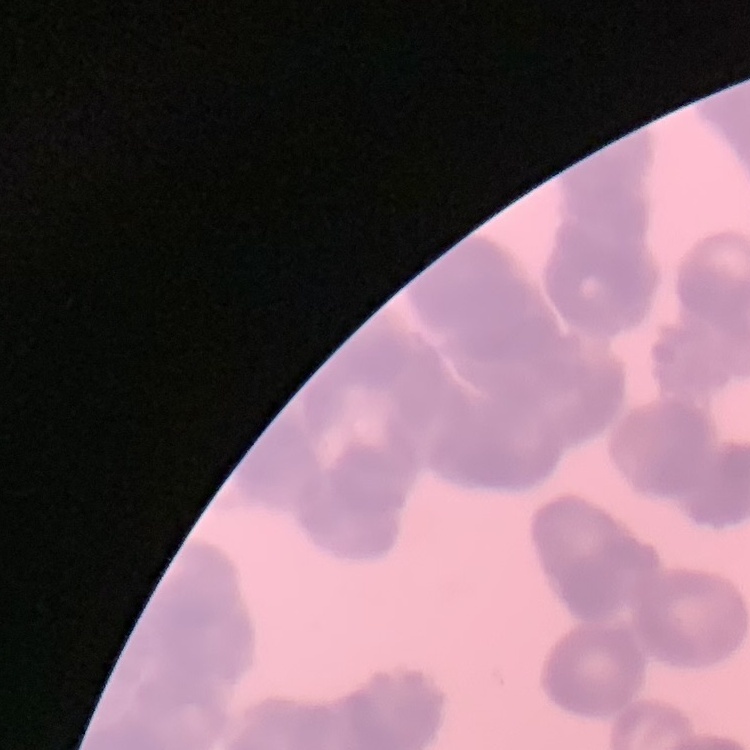

Summary:
  - Red blood cell morphology: rouleaux formation
  - Stain: Field's or Giemsa
  - Image type: one tile cut from a larger photomicrograph
  - Preparation: thin peripheral smear